State which cell type is depicted.
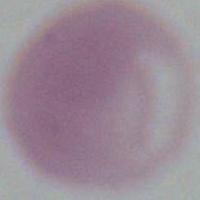
This is an erythrocyte.

magnification = 1000x
modality = micrograph